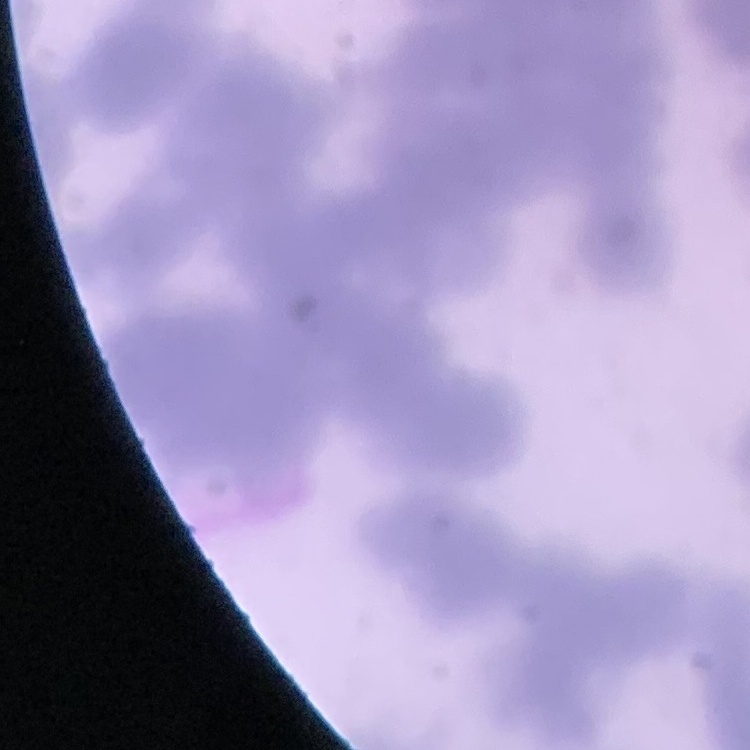
Summary:
  - Erythrocyte morphology: rouleaux formation
  - Image type: square crop of a larger photomicrograph
  - Stain: Field's or Giemsa
  - Preparation: thin peripheral smear